Locate the P. falciparum-infected red blood cells and any of indeterminate infection status.
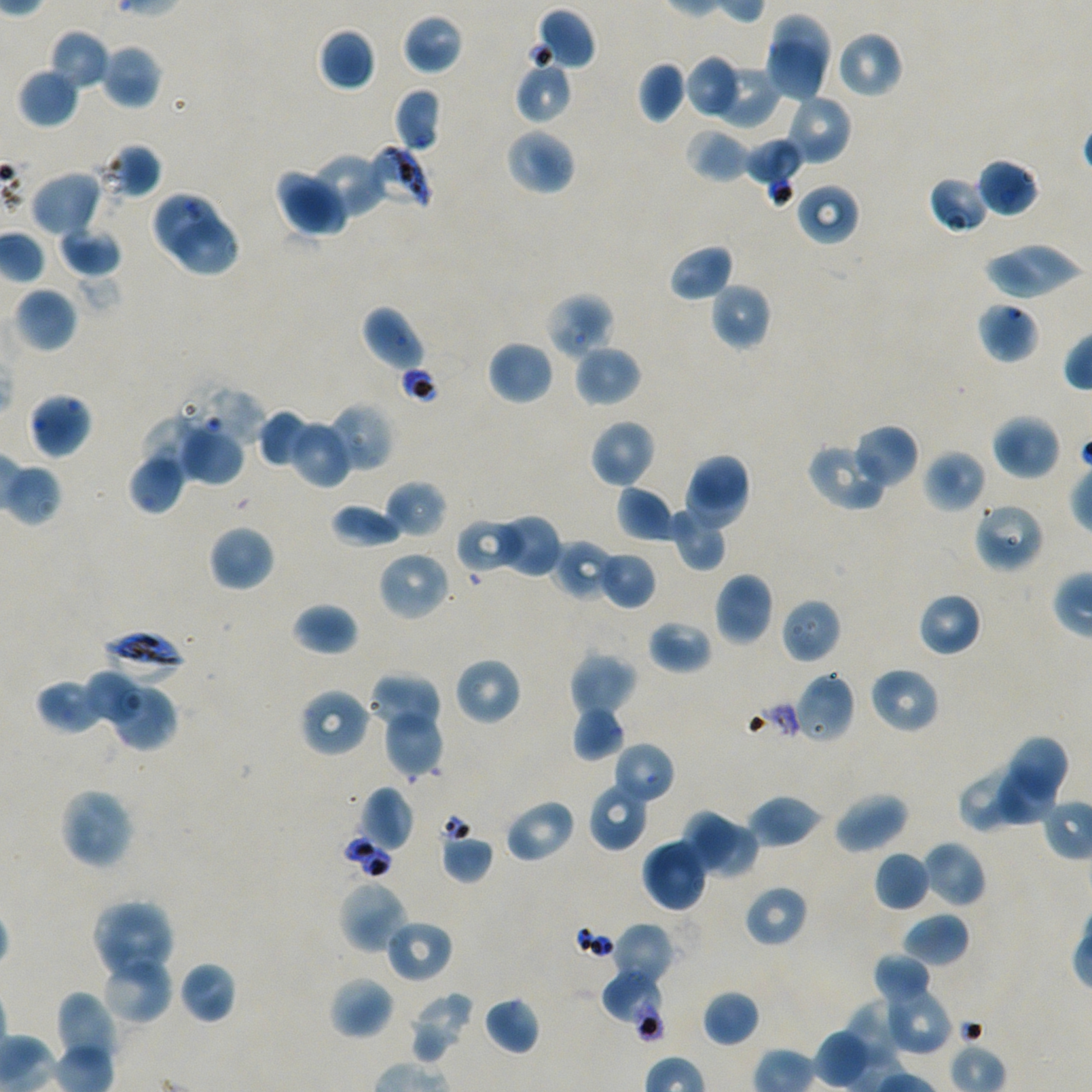

Approximate bounding rectangles given as corner coordinates in pixels from the top-left. Not every red blood cell is marked.
Infected red blood cells: (x1=365, y1=144, x2=432, y2=211), (x1=101, y1=629, x2=186, y2=679).
Red blood cells of indeterminate infection status: (x1=98, y1=143, x2=162, y2=200), (x1=150, y1=189, x2=224, y2=259), (x1=977, y1=301, x2=1040, y2=364), (x1=600, y1=966, x2=668, y2=1042).

Locations of uninfected red blood cells: (x1=534, y1=7, x2=597, y2=71), (x1=771, y1=12, x2=833, y2=75), (x1=402, y1=14, x2=464, y2=75), (x1=318, y1=26, x2=376, y2=92), (x1=49, y1=30, x2=109, y2=91), (x1=834, y1=30, x2=903, y2=99), (x1=763, y1=41, x2=824, y2=103), (x1=101, y1=44, x2=161, y2=109), (x1=684, y1=55, x2=742, y2=119), (x1=514, y1=59, x2=572, y2=124), (x1=706, y1=60, x2=782, y2=127), (x1=637, y1=61, x2=687, y2=122), (x1=18, y1=68, x2=79, y2=128), (x1=393, y1=88, x2=442, y2=153), (x1=785, y1=94, x2=852, y2=166), (x1=684, y1=127, x2=750, y2=184), (x1=505, y1=128, x2=576, y2=196), (x1=742, y1=137, x2=803, y2=192), (x1=308, y1=150, x2=386, y2=221), (x1=977, y1=157, x2=1040, y2=218), (x1=276, y1=168, x2=350, y2=237), (x1=29, y1=169, x2=103, y2=238), (x1=928, y1=175, x2=991, y2=234), (x1=795, y1=182, x2=859, y2=246), (x1=168, y1=219, x2=242, y2=278), (x1=58, y1=226, x2=122, y2=277), (x1=980, y1=242, x2=1086, y2=302), (x1=668, y1=243, x2=734, y2=302), (x1=710, y1=282, x2=771, y2=350), (x1=14, y1=287, x2=77, y2=353), (x1=545, y1=292, x2=616, y2=359), (x1=360, y1=305, x2=425, y2=372), (x1=488, y1=340, x2=553, y2=405), (x1=574, y1=344, x2=641, y2=407), (x1=193, y1=386, x2=269, y2=445), (x1=26, y1=392, x2=92, y2=459), (x1=329, y1=403, x2=393, y2=471), (x1=257, y1=410, x2=311, y2=468), (x1=991, y1=413, x2=1061, y2=480), (x1=136, y1=416, x2=195, y2=487), (x1=288, y1=419, x2=353, y2=488), (x1=589, y1=419, x2=657, y2=489), (x1=852, y1=423, x2=920, y2=488), (x1=180, y1=424, x2=244, y2=484), (x1=808, y1=442, x2=889, y2=510), (x1=922, y1=449, x2=987, y2=513), (x1=130, y1=454, x2=186, y2=515), (x1=683, y1=454, x2=752, y2=532), (x1=0, y1=460, x2=63, y2=527), (x1=385, y1=480, x2=447, y2=539), (x1=616, y1=485, x2=676, y2=543), (x1=330, y1=502, x2=405, y2=549), (x1=972, y1=502, x2=1046, y2=574), (x1=670, y1=507, x2=727, y2=571), (x1=490, y1=514, x2=562, y2=579), (x1=456, y1=517, x2=526, y2=576), (x1=208, y1=525, x2=275, y2=592), (x1=553, y1=539, x2=616, y2=601), (x1=377, y1=550, x2=450, y2=621), (x1=596, y1=551, x2=657, y2=609), (x1=713, y1=572, x2=774, y2=647), (x1=917, y1=592, x2=983, y2=657), (x1=781, y1=597, x2=841, y2=664), (x1=292, y1=602, x2=359, y2=657), (x1=647, y1=619, x2=713, y2=675), (x1=569, y1=652, x2=638, y2=718), (x1=454, y1=657, x2=522, y2=726), (x1=869, y1=666, x2=940, y2=734), (x1=367, y1=671, x2=441, y2=731), (x1=87, y1=672, x2=143, y2=726), (x1=794, y1=672, x2=855, y2=744), (x1=35, y1=677, x2=108, y2=734), (x1=115, y1=684, x2=177, y2=751), (x1=299, y1=688, x2=371, y2=758), (x1=571, y1=704, x2=626, y2=761), (x1=383, y1=710, x2=443, y2=778), (x1=1008, y1=737, x2=1068, y2=794), (x1=612, y1=742, x2=676, y2=807), (x1=997, y1=761, x2=1055, y2=825), (x1=958, y1=776, x2=1013, y2=834), (x1=588, y1=781, x2=651, y2=852), (x1=359, y1=785, x2=414, y2=852), (x1=58, y1=786, x2=135, y2=869), (x1=833, y1=792, x2=910, y2=854), (x1=746, y1=795, x2=822, y2=848), (x1=503, y1=797, x2=576, y2=864), (x1=681, y1=807, x2=739, y2=872), (x1=702, y1=824, x2=757, y2=880), (x1=440, y1=833, x2=494, y2=884), (x1=641, y1=838, x2=708, y2=913), (x1=922, y1=840, x2=987, y2=909), (x1=873, y1=850, x2=932, y2=912), (x1=338, y1=879, x2=410, y2=954), (x1=743, y1=884, x2=808, y2=947), (x1=91, y1=899, x2=175, y2=982), (x1=903, y1=913, x2=970, y2=967), (x1=384, y1=917, x2=453, y2=983), (x1=613, y1=922, x2=674, y2=987), (x1=872, y1=952, x2=934, y2=1008), (x1=101, y1=953, x2=173, y2=1025), (x1=179, y1=960, x2=237, y2=1024), (x1=328, y1=976, x2=395, y2=1040), (x1=880, y1=985, x2=951, y2=1055), (x1=55, y1=989, x2=117, y2=1074), (x1=702, y1=989, x2=761, y2=1047), (x1=408, y1=991, x2=476, y2=1065), (x1=483, y1=995, x2=541, y2=1056), (x1=843, y1=1001, x2=903, y2=1070), (x1=816, y1=1029, x2=869, y2=1089). One field from this slide. Image is 1092×1092 pixels. Thin blood film. Oil immersion, 100x objective (numerical aperture 1.45). Blood group of the donor: A+/O+. Static in-vitro culture of P. falciparum strain NF54. Giemsa-stained preparation.